Assess the morphology of the red blood cells.
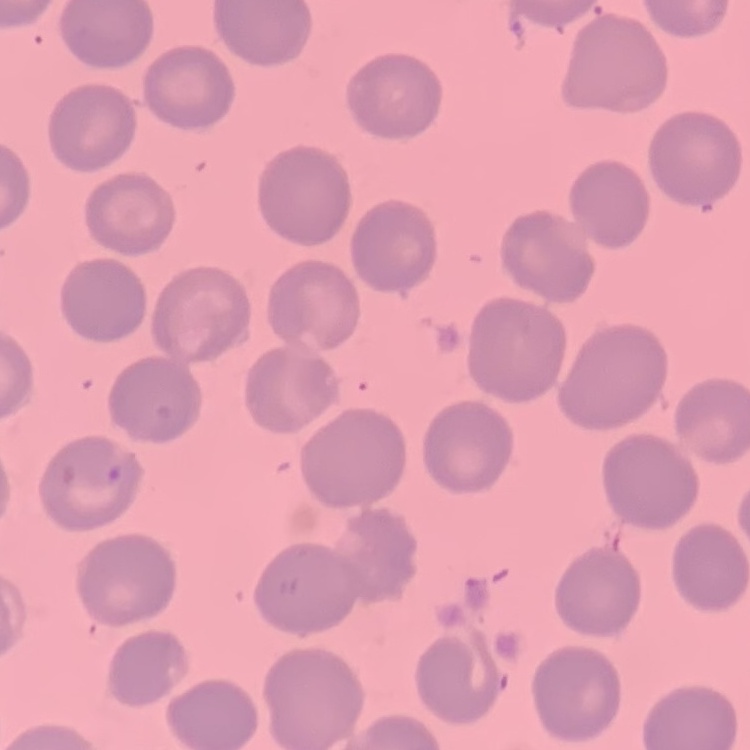

They show no rouleaux formation.

Thin blood smear. Square crop of a larger photomicrograph. Stained with either Field's or Giemsa.